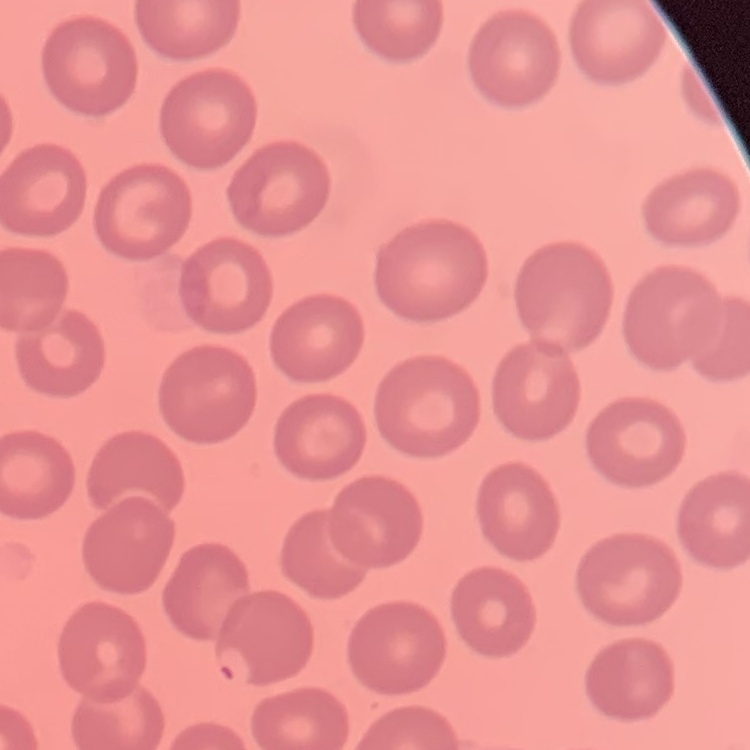

Summary:
  - Red blood cell morphology: no rouleaux formation
  - Stain: Field's or Giemsa
  - Preparation: thin blood film
  - Image type: one tile cut from a larger photomicrograph